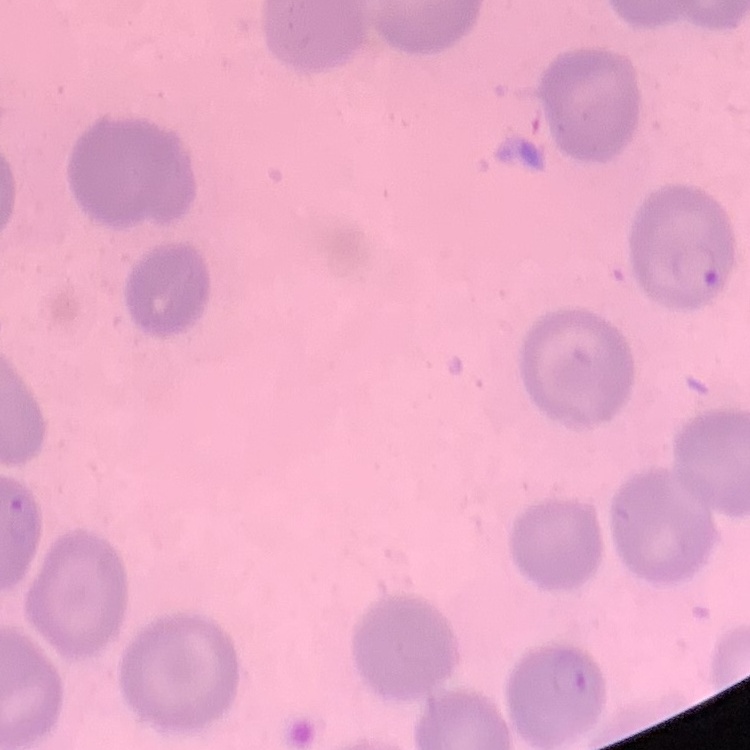
Summary:
  - Erythrocyte morphology: no rouleaux formation
  - Preparation: thin blood smear
  - Stain: Field's or Giemsa
  - Image type: square crop of a larger photomicrograph